Assess the morphology of the red blood cells.
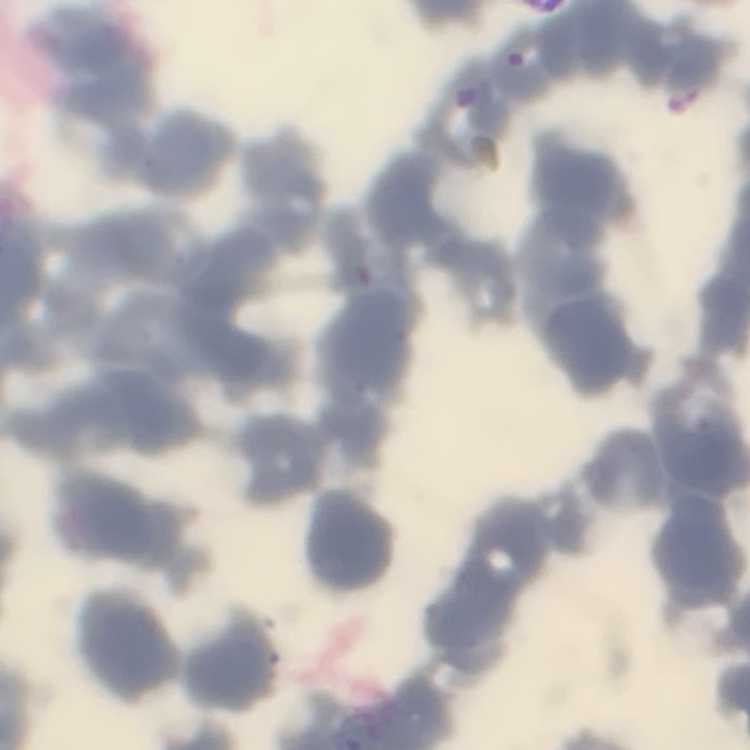
Rouleaux formation.

Summary:
  - Preparation: thin peripheral smear
  - Image type: one tile cut from a larger photomicrograph
  - Stain: Field's or Giemsa